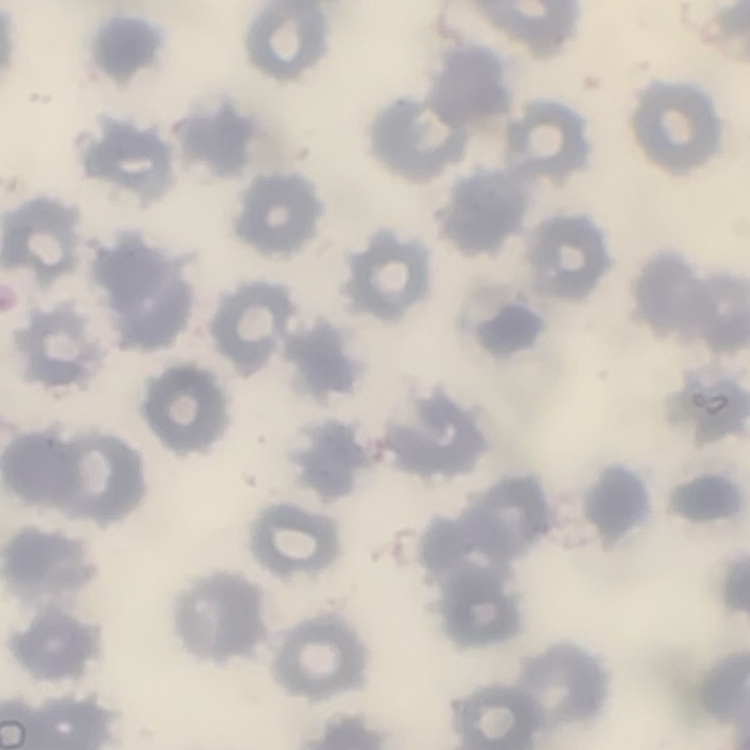
The erythrocytes exhibit no rouleaux formation. Field's or Giemsa stain. One tile cut from a larger photomicrograph. Thin blood film.